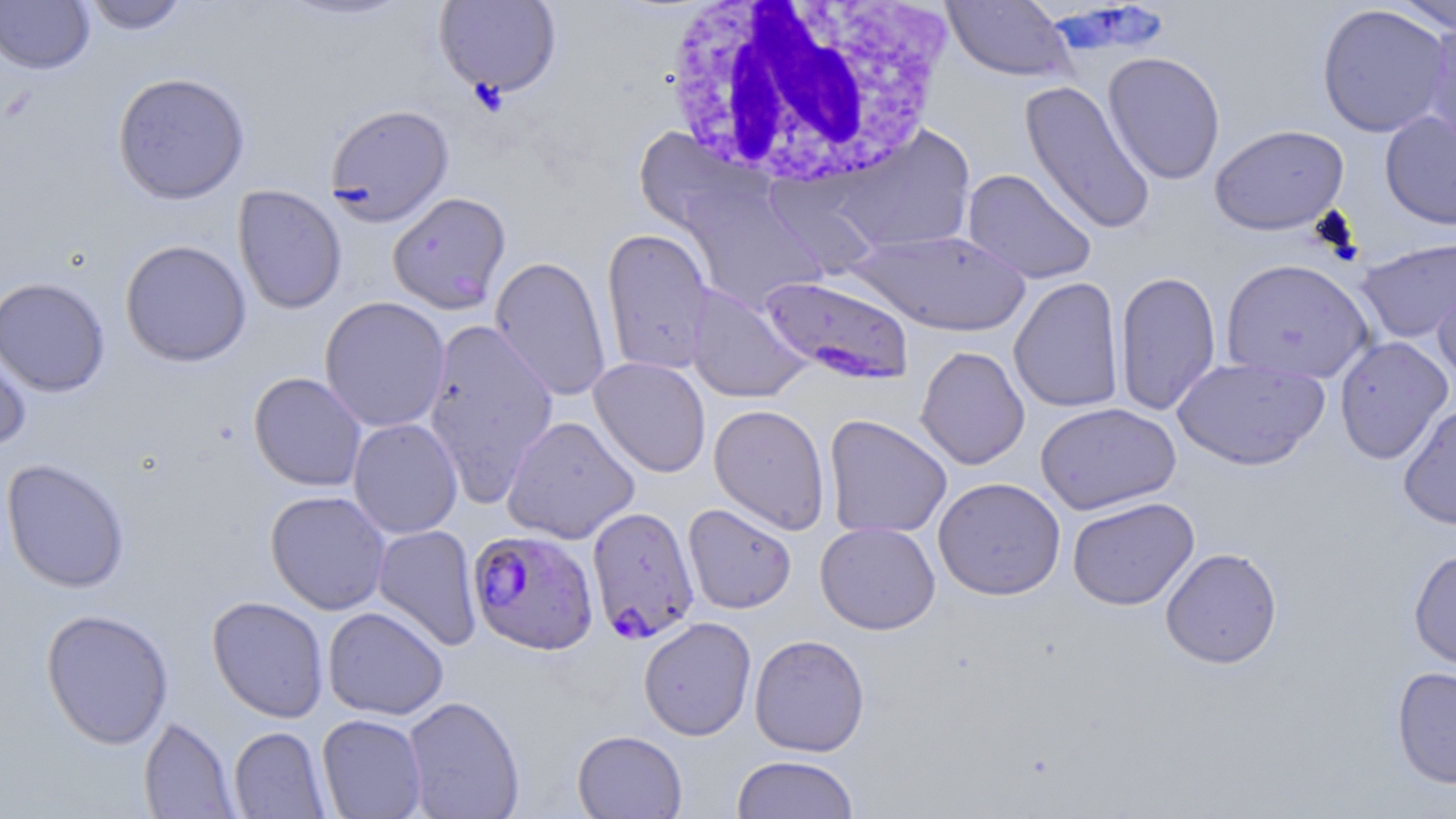

slide_level_diagnosis: Plasmodium falciparum
white_blood_cell_locations: 'approximate bounding boxes as named x1/y1/x2/y2 corners in pixels: (x1=661, y1=0, x2=950, y2=191)'
uninfected_red_blood_cell_locations: 'approximate bounding boxes as named x1/y1/x2/y2 corners in pixels: (x1=82, y1=0, x2=190, y2=34), (x1=433, y1=0, x2=563, y2=97), (x1=942, y1=0, x2=1074, y2=82), (x1=1388, y1=0, x2=1456, y2=35), (x1=0, y1=1, x2=94, y2=74), (x1=1316, y1=3, x2=1452, y2=138), (x1=1420, y1=19, x2=1456, y2=158), (x1=1103, y1=51, x2=1226, y2=185), (x1=112, y1=72, x2=250, y2=205), (x1=1019, y1=80, x2=1157, y2=236), (x1=325, y1=103, x2=454, y2=225), (x1=1379, y1=111, x2=1456, y2=230), (x1=1210, y1=124, x2=1349, y2=235), (x1=835, y1=125, x2=977, y2=255), (x1=632, y1=128, x2=765, y2=235), (x1=962, y1=168, x2=1097, y2=285), (x1=676, y1=181, x2=825, y2=312), (x1=233, y1=185, x2=347, y2=315), (x1=388, y1=191, x2=511, y2=314), (x1=601, y1=227, x2=715, y2=376), (x1=850, y1=229, x2=1032, y2=337), (x1=1356, y1=238, x2=1455, y2=343), (x1=120, y1=239, x2=252, y2=367), (x1=490, y1=256, x2=612, y2=403), (x1=1220, y1=258, x2=1374, y2=383), (x1=1431, y1=266, x2=1456, y2=386), (x1=1114, y1=269, x2=1222, y2=416), (x1=1008, y1=276, x2=1124, y2=413), (x1=0, y1=277, x2=111, y2=397), (x1=684, y1=284, x2=811, y2=404), (x1=319, y1=296, x2=451, y2=432), (x1=422, y1=319, x2=559, y2=505), (x1=0, y1=329, x2=33, y2=453), (x1=1334, y1=336, x2=1454, y2=465), (x1=915, y1=345, x2=1030, y2=470), (x1=1172, y1=356, x2=1329, y2=470), (x1=589, y1=357, x2=711, y2=478), (x1=248, y1=371, x2=367, y2=492), (x1=1035, y1=402, x2=1181, y2=515), (x1=1398, y1=403, x2=1456, y2=531), (x1=708, y1=404, x2=831, y2=535), (x1=823, y1=414, x2=952, y2=540), (x1=502, y1=415, x2=640, y2=544), (x1=348, y1=417, x2=463, y2=539), (x1=1, y1=458, x2=130, y2=593), (x1=933, y1=477, x2=1066, y2=600), (x1=265, y1=490, x2=391, y2=615), (x1=1067, y1=496, x2=1199, y2=611), (x1=683, y1=503, x2=796, y2=614), (x1=815, y1=521, x2=941, y2=634), (x1=372, y1=524, x2=482, y2=651), (x1=1160, y1=547, x2=1283, y2=669), (x1=1408, y1=547, x2=1456, y2=672), (x1=207, y1=595, x2=329, y2=723), (x1=322, y1=605, x2=449, y2=720), (x1=40, y1=608, x2=175, y2=749), (x1=638, y1=616, x2=756, y2=740), (x1=749, y1=633, x2=870, y2=757), (x1=1391, y1=665, x2=1456, y2=789), (x1=402, y1=695, x2=525, y2=818), (x1=316, y1=713, x2=428, y2=818), (x1=139, y1=716, x2=239, y2=818), (x1=228, y1=726, x2=331, y2=818), (x1=572, y1=730, x2=687, y2=818), (x1=731, y1=754, x2=860, y2=819)'
image_size: 1456×819 pixels
stain: May-Grünwald-Giemsa
preparation: thin blood film
plasmodium_falciparum_infected_red_blood_cell_locations: 'approximate bounding boxes as named x1/y1/x2/y2 corners in pixels: (x1=758, y1=274, x2=915, y2=385), (x1=587, y1=505, x2=699, y2=644), (x1=467, y1=529, x2=599, y2=655)'
modality: optical microscopy
field_of_view: one of a larger specimen
magnification: 1000x